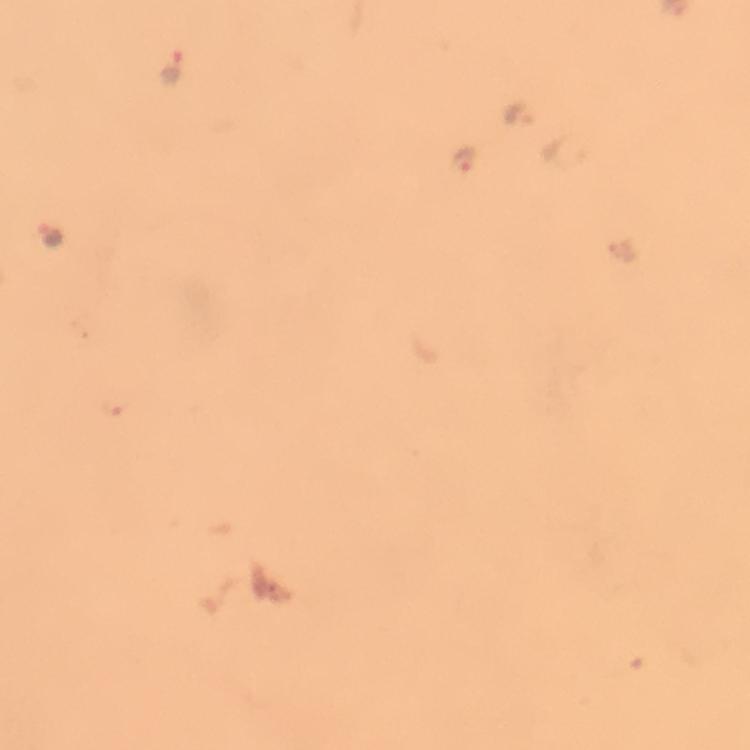 Approximate object centers, in pixels from the top-left corner. Malaria parasite locations: (x=174, y=67), (x=520, y=111), (x=468, y=161), (x=49, y=234). Immersion oil applied. Giemsa stain. A crop from one field of view. Image is 750×750 pixels. Thick blood smear. Photographed with a smartphone mounted on the microscope. From a diagnostic examination for malaria. 100x magnification.